Assess this cell for malaria.
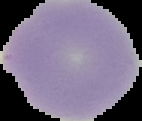
It is uninfected.

From a thin blood film. The area outside the segmented cell region is set to black. Image is 142×121 pixels.